Outline each Trypanosoma brucei.
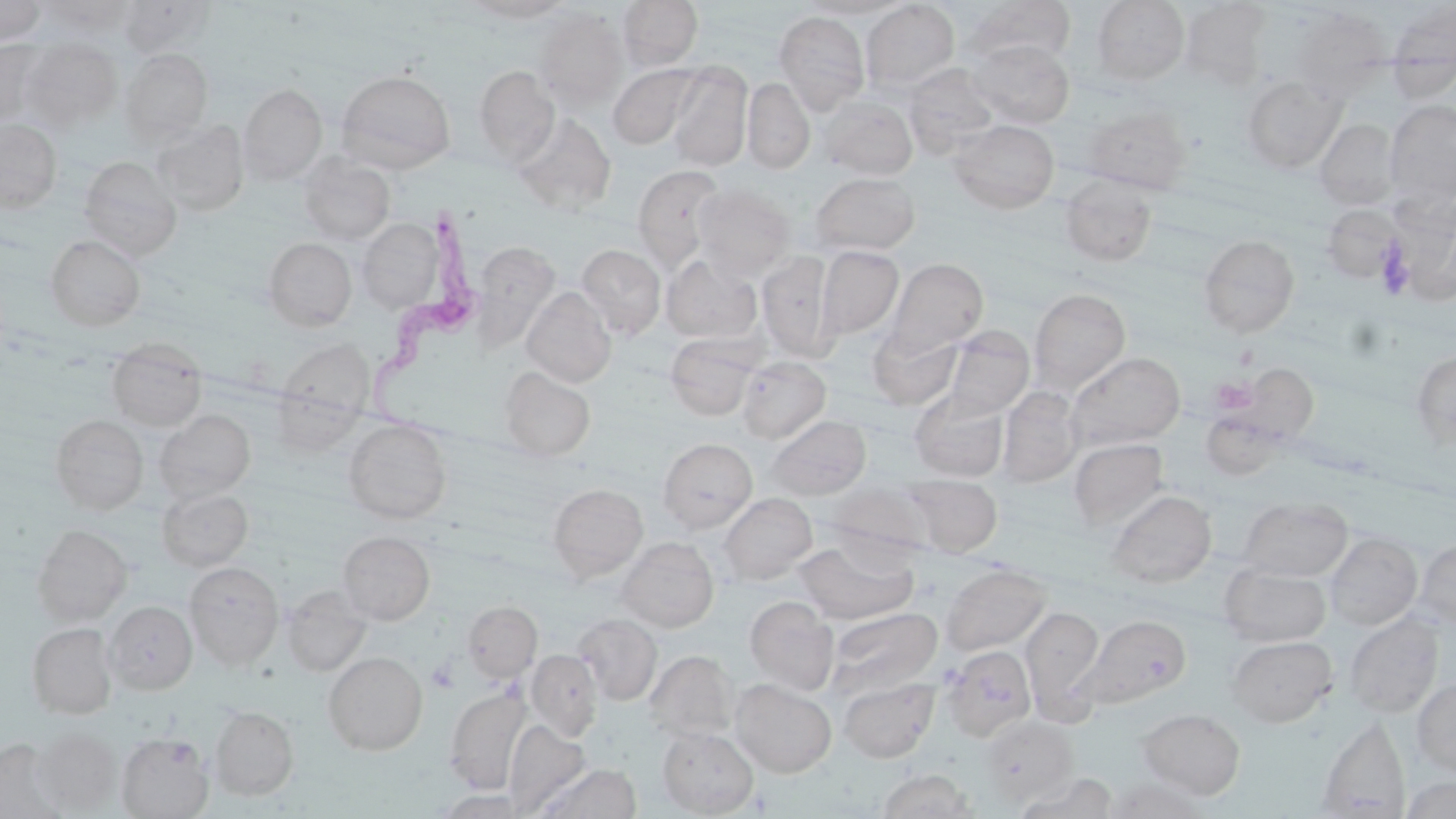

Approximate bounding boxes as named x1/y1/x2/y2 corners in pixels.
Trypanosoma brucei: (x1=365, y1=196, x2=479, y2=440).

Summary:
  - Uninfected red blood cell locations: (x1=39, y1=0, x2=138, y2=36), (x1=117, y1=0, x2=213, y2=57), (x1=617, y1=0, x2=703, y2=71), (x1=964, y1=0, x2=1076, y2=65), (x1=1092, y1=0, x2=1189, y2=86), (x1=0, y1=1, x2=47, y2=44), (x1=461, y1=1, x2=574, y2=22), (x1=799, y1=1, x2=910, y2=19), (x1=862, y1=1, x2=959, y2=94), (x1=1179, y1=1, x2=1272, y2=90), (x1=1386, y1=3, x2=1456, y2=100), (x1=1291, y1=7, x2=1392, y2=101), (x1=534, y1=8, x2=628, y2=109), (x1=774, y1=11, x2=870, y2=114), (x1=21, y1=37, x2=123, y2=131), (x1=0, y1=39, x2=57, y2=127), (x1=968, y1=39, x2=1074, y2=128), (x1=120, y1=49, x2=212, y2=145), (x1=608, y1=63, x2=703, y2=149), (x1=667, y1=63, x2=752, y2=170), (x1=902, y1=63, x2=1000, y2=157), (x1=475, y1=65, x2=560, y2=164), (x1=336, y1=69, x2=455, y2=173), (x1=1241, y1=75, x2=1347, y2=173), (x1=742, y1=78, x2=815, y2=173), (x1=239, y1=83, x2=326, y2=183), (x1=818, y1=96, x2=918, y2=180), (x1=1385, y1=99, x2=1456, y2=204), (x1=1082, y1=105, x2=1192, y2=194), (x1=512, y1=113, x2=617, y2=213), (x1=0, y1=118, x2=62, y2=212), (x1=1315, y1=118, x2=1399, y2=210), (x1=948, y1=119, x2=1059, y2=213), (x1=153, y1=120, x2=249, y2=216), (x1=298, y1=155, x2=395, y2=244), (x1=78, y1=157, x2=182, y2=260), (x1=631, y1=164, x2=727, y2=270), (x1=811, y1=172, x2=920, y2=255), (x1=1060, y1=175, x2=1157, y2=266), (x1=693, y1=184, x2=795, y2=280), (x1=1320, y1=204, x2=1403, y2=283), (x1=357, y1=218, x2=444, y2=312), (x1=1198, y1=234, x2=1300, y2=338), (x1=45, y1=235, x2=145, y2=331), (x1=263, y1=237, x2=357, y2=331), (x1=470, y1=241, x2=560, y2=351), (x1=577, y1=244, x2=666, y2=338), (x1=817, y1=245, x2=903, y2=339), (x1=758, y1=251, x2=836, y2=361), (x1=662, y1=255, x2=762, y2=343), (x1=883, y1=258, x2=988, y2=359), (x1=521, y1=287, x2=616, y2=388), (x1=1029, y1=287, x2=1130, y2=393), (x1=869, y1=325, x2=964, y2=409), (x1=942, y1=326, x2=1034, y2=420), (x1=665, y1=334, x2=761, y2=420), (x1=107, y1=338, x2=207, y2=432), (x1=276, y1=338, x2=375, y2=427), (x1=1411, y1=349, x2=1456, y2=450), (x1=1065, y1=351, x2=1186, y2=451), (x1=737, y1=356, x2=831, y2=443), (x1=1231, y1=363, x2=1319, y2=445), (x1=499, y1=366, x2=596, y2=461), (x1=997, y1=386, x2=1083, y2=487), (x1=910, y1=390, x2=1010, y2=483), (x1=155, y1=409, x2=255, y2=502), (x1=50, y1=414, x2=149, y2=514), (x1=766, y1=415, x2=871, y2=499), (x1=344, y1=419, x2=451, y2=523), (x1=658, y1=438, x2=757, y2=533), (x1=1068, y1=438, x2=1169, y2=531), (x1=904, y1=474, x2=1002, y2=556), (x1=548, y1=482, x2=647, y2=580), (x1=824, y1=482, x2=933, y2=560), (x1=157, y1=487, x2=253, y2=571), (x1=1107, y1=490, x2=1216, y2=588), (x1=719, y1=493, x2=817, y2=584), (x1=1239, y1=497, x2=1352, y2=581), (x1=31, y1=524, x2=132, y2=626), (x1=337, y1=531, x2=435, y2=624), (x1=1324, y1=533, x2=1423, y2=630), (x1=616, y1=537, x2=719, y2=632), (x1=794, y1=539, x2=917, y2=624), (x1=1414, y1=539, x2=1456, y2=629), (x1=184, y1=561, x2=284, y2=669), (x1=940, y1=563, x2=1051, y2=656), (x1=1220, y1=563, x2=1331, y2=646), (x1=282, y1=586, x2=371, y2=676), (x1=745, y1=597, x2=839, y2=695), (x1=463, y1=600, x2=542, y2=682), (x1=105, y1=601, x2=197, y2=695), (x1=1020, y1=605, x2=1105, y2=719), (x1=825, y1=607, x2=942, y2=698), (x1=574, y1=614, x2=662, y2=705), (x1=1344, y1=614, x2=1444, y2=717), (x1=1078, y1=615, x2=1191, y2=708), (x1=27, y1=622, x2=117, y2=719), (x1=1227, y1=635, x2=1337, y2=727), (x1=941, y1=645, x2=1036, y2=741), (x1=527, y1=649, x2=603, y2=740), (x1=645, y1=650, x2=738, y2=741), (x1=323, y1=652, x2=427, y2=756), (x1=838, y1=676, x2=939, y2=763), (x1=731, y1=679, x2=837, y2=777), (x1=1412, y1=679, x2=1456, y2=776), (x1=443, y1=687, x2=532, y2=794), (x1=210, y1=706, x2=299, y2=800), (x1=1137, y1=708, x2=1245, y2=799), (x1=980, y1=715, x2=1077, y2=804), (x1=1316, y1=716, x2=1411, y2=818), (x1=503, y1=720, x2=589, y2=817), (x1=657, y1=726, x2=758, y2=816), (x1=33, y1=728, x2=120, y2=814), (x1=116, y1=732, x2=214, y2=818), (x1=0, y1=738, x2=66, y2=819), (x1=534, y1=762, x2=641, y2=819), (x1=876, y1=770, x2=977, y2=818), (x1=1013, y1=772, x2=1120, y2=818), (x1=1104, y1=774, x2=1209, y2=818), (x1=1402, y1=776, x2=1455, y2=819), (x1=434, y1=789, x2=529, y2=818)
  - Platelet locations: (x1=1377, y1=244, x2=1415, y2=299), (x1=1211, y1=377, x2=1257, y2=414), (x1=427, y1=661, x2=459, y2=693)
  - Slide-level diagnosis: Trypanosoma brucei
  - Magnification: 1000x
  - Field of view: single
  - Stain: May-Grünwald-Giemsa
  - Image size: 1456×819 pixels
  - Modality: optical microscopy
  - Preparation: thin blood film